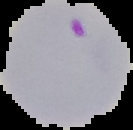 Image is 133×130 pixels. The area outside the segmented cell region is set to black. Malaria status: parasitized. From a thin blood smear.